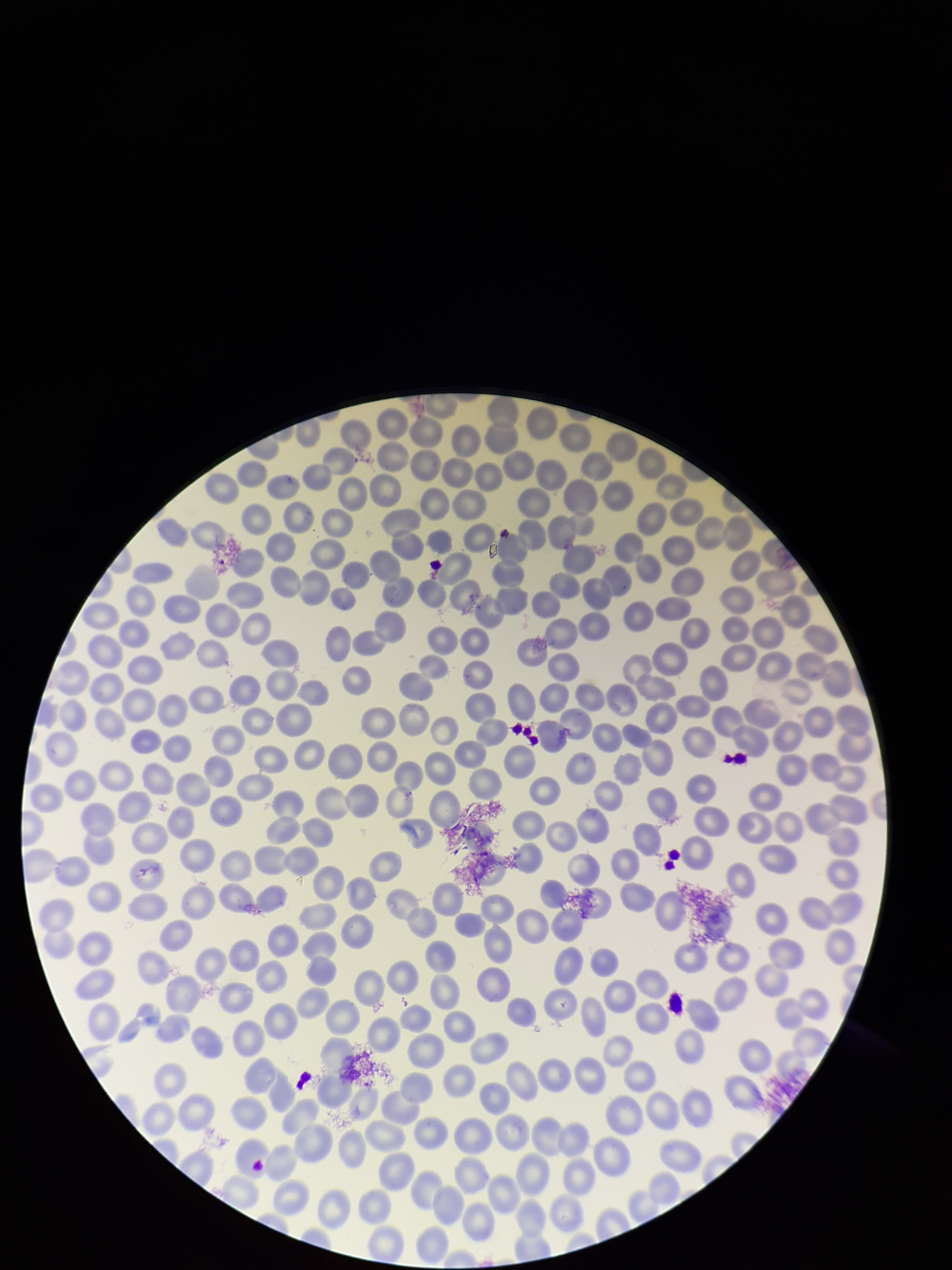
patient malaria status = negative
parasitized red blood cell count = 0
parasitized red blood cells = none seen
stain = Giemsa
field of view = one from this slide
capture = smartphone photograph through the microscope eyepiece
red blood cell count = 312
preparation = thin smear
image size = 952×1270 pixels